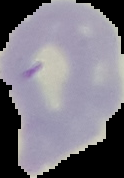

Summary:
  - Image size: 124×178 pixels
  - Malaria status: uninfected
  - Image type: segmented cell region on a black background
  - Preparation: thin blood film